Find the red blood cells and label each as Plasmodium falciparum-infected, uninfected, or of indeterminate infection status.
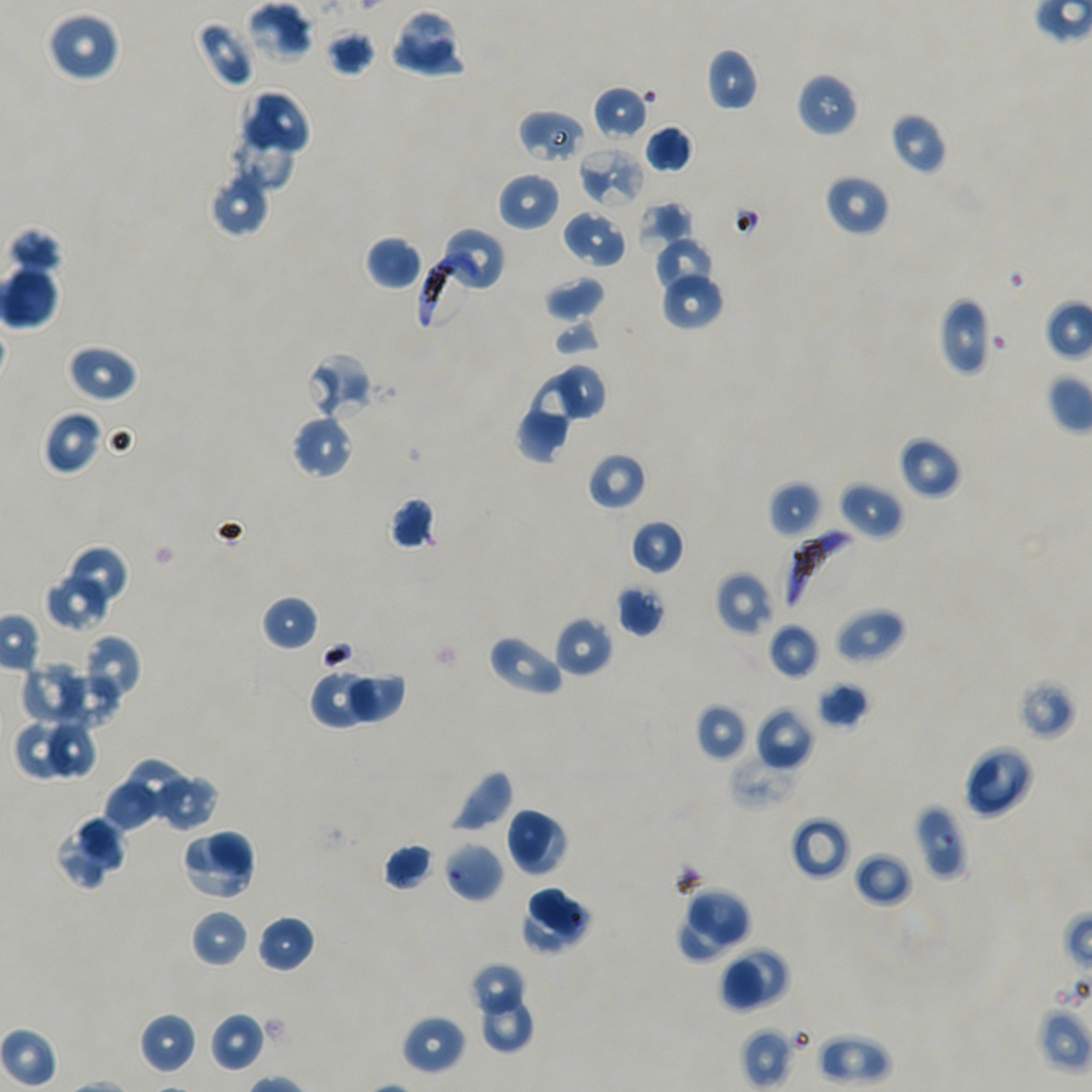
Approximate bounding boxes as [x1, y1, x2, y2] in pixels. Not every red blood cell is marked.
Infected red blood cells: [418, 251, 472, 330], [783, 529, 855, 613].
Red blood cells of indeterminate infection status: [517, 109, 586, 164], [578, 145, 646, 209], [306, 352, 373, 420], [913, 803, 968, 881].
Uninfected red blood cells: [245, 2, 314, 63], [399, 8, 455, 65], [46, 11, 121, 83], [195, 20, 257, 90], [325, 27, 377, 77], [392, 41, 469, 78], [705, 47, 759, 112], [796, 71, 858, 137], [592, 86, 650, 141], [240, 89, 312, 159], [888, 111, 947, 175], [230, 114, 293, 190], [644, 124, 693, 174], [212, 172, 267, 238], [496, 172, 560, 232], [824, 173, 890, 236], [636, 201, 692, 249], [562, 208, 629, 269], [437, 225, 507, 295], [11, 230, 58, 279], [365, 236, 422, 290], [654, 237, 714, 293], [0, 246, 62, 329], [661, 271, 725, 330], [544, 276, 606, 323], [937, 297, 991, 376], [552, 318, 601, 357], [65, 343, 137, 403], [560, 363, 606, 421], [527, 371, 581, 443], [41, 410, 102, 475], [514, 412, 569, 464], [291, 413, 354, 480], [898, 435, 962, 499], [587, 452, 647, 511], [767, 480, 824, 539], [838, 481, 904, 541], [388, 496, 437, 551], [629, 520, 685, 576], [63, 545, 130, 611], [44, 570, 112, 632], [714, 571, 774, 637], [615, 583, 666, 637], [261, 594, 318, 651], [835, 607, 905, 664], [554, 617, 614, 678], [767, 623, 820, 680], [487, 634, 564, 697], [84, 635, 141, 703], [22, 661, 94, 727], [58, 663, 122, 729], [309, 669, 380, 730], [348, 674, 406, 725], [1016, 677, 1077, 741], [815, 681, 870, 729], [695, 702, 748, 761], [755, 707, 814, 771], [14, 721, 67, 781], [50, 721, 95, 778], [962, 745, 1034, 818], [729, 754, 803, 811], [120, 759, 192, 820], [445, 767, 514, 834], [151, 772, 220, 833], [105, 781, 157, 828], [505, 807, 569, 876], [52, 815, 128, 890], [789, 816, 851, 881], [179, 829, 257, 901], [443, 841, 505, 903], [382, 842, 435, 891], [852, 850, 913, 908], [528, 886, 593, 942], [687, 886, 752, 947], [526, 900, 591, 958], [189, 909, 249, 968], [257, 915, 315, 973], [678, 915, 731, 962], [731, 947, 789, 1002], [722, 959, 765, 1013], [469, 964, 526, 1017], [469, 964, 533, 1051], [483, 994, 532, 1052], [139, 1012, 198, 1074], [209, 1012, 266, 1072], [401, 1014, 466, 1076], [740, 1027, 793, 1090], [816, 1033, 892, 1087].

Thin blood smear. Giemsa-stained preparation. One field from this slide. Image is 1092×1092 pixels. Static in-vitro culture of Plasmodium falciparum strain NF54. Blood group of the donor: A+/O+. 100x oil-immersion objective, numerical aperture 1.45.